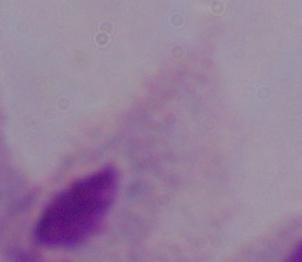

Summary:
  - Identification: trichomonad
  - Modality: micrograph
  - Magnification: 1000x